Mark where leukocytes are.
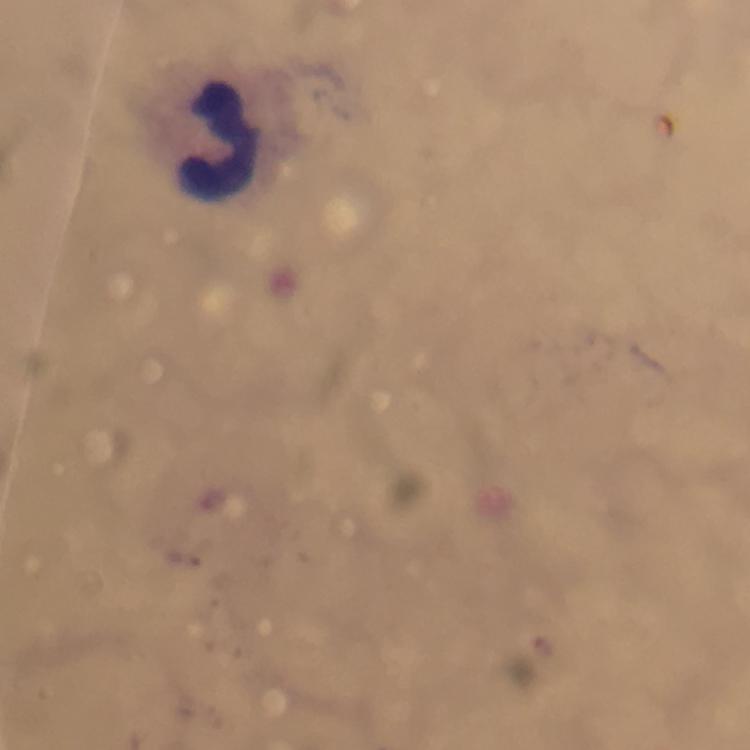
Approximate centers as [x, y] in pixels.
Leukocytes: [219, 140].

Summary:
  - Context: from a malaria diagnostic workup
  - Image size: 750×750 pixels
  - Cropped from: a single field of view
  - Stain: Giemsa
  - Plasmodium parasites: none detected
  - Capture: smartphone mounted on the microscope
  - Preparation: thick blood smear
  - Magnification: 100x
  - Immersion oil: used